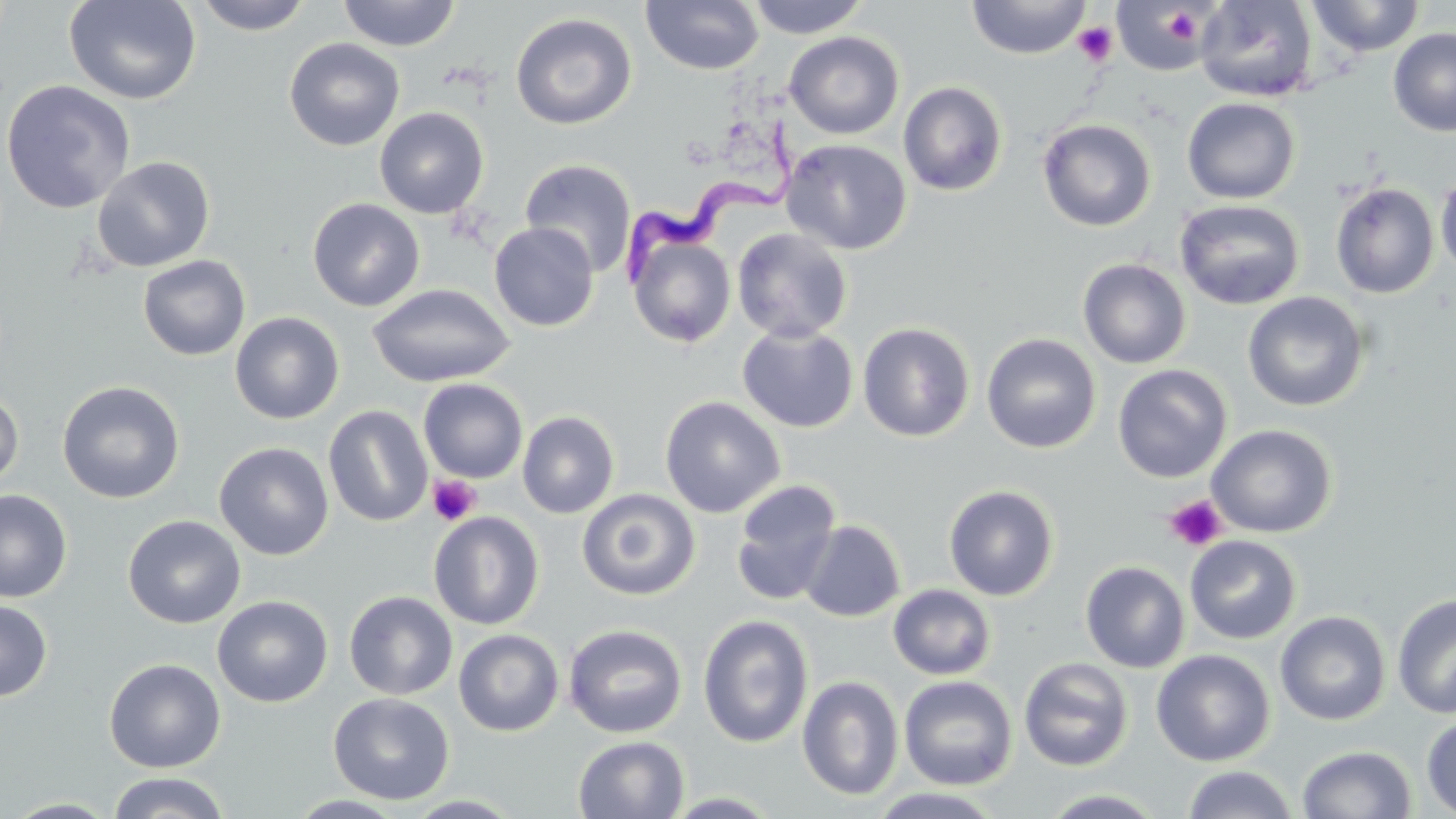

slide_level_diagnosis: Trypanosoma brucei
modality: light microscopy
magnification: 1000x
trypanosoma_brucei_locations: 'approximate bounding boxes as [x1, y1, x2, y2] in pixels: [622, 115, 807, 292]'
field_of_view: one of a larger specimen
preparation: thin blood smear
platelet_locations: 'approximate bounding boxes as [x1, y1, x2, y2] in pixels: [1162, 7, 1203, 47], [1072, 21, 1118, 66], [427, 475, 481, 526], [1164, 495, 1228, 552]'
stain: May-Grünwald-Giemsa
image_size: 1456×819 pixels
uninfected_red_blood_cell_locations: 'approximate bounding boxes as [x1, y1, x2, y2] in pixels: [63, 0, 202, 105], [192, 0, 314, 35], [337, 0, 460, 51], [641, 0, 764, 76], [745, 0, 871, 39], [966, 0, 1091, 60], [1112, 0, 1218, 76], [1194, 0, 1317, 102], [1306, 0, 1425, 57], [510, 12, 637, 130], [1388, 27, 1456, 136], [784, 31, 904, 140], [284, 37, 405, 152], [0, 79, 136, 214], [898, 81, 1008, 196], [1182, 97, 1301, 204], [374, 107, 490, 219], [1037, 118, 1156, 231], [781, 138, 912, 255], [91, 155, 216, 272], [519, 158, 637, 277], [1435, 170, 1456, 278], [1330, 182, 1440, 299], [307, 197, 426, 311], [1174, 198, 1305, 310], [488, 222, 599, 332], [732, 228, 853, 343], [626, 230, 736, 350], [137, 255, 250, 361], [1078, 258, 1192, 369], [367, 282, 515, 388], [1242, 291, 1370, 412], [229, 312, 345, 425], [858, 322, 975, 442], [737, 323, 858, 433], [981, 332, 1101, 453], [1112, 364, 1232, 483], [418, 378, 528, 483], [57, 380, 185, 504], [0, 387, 24, 492], [660, 396, 785, 517], [323, 405, 433, 527], [517, 411, 620, 519], [1207, 423, 1338, 538], [214, 442, 334, 560], [730, 480, 844, 606], [943, 484, 1059, 601], [577, 487, 700, 600], [0, 489, 73, 602], [428, 510, 544, 630], [123, 514, 246, 629], [799, 520, 906, 622], [1184, 535, 1302, 644], [1080, 560, 1190, 673], [888, 584, 997, 680], [344, 590, 458, 700], [1392, 593, 1456, 719], [212, 595, 333, 707], [0, 599, 53, 701], [1275, 610, 1391, 726], [697, 614, 814, 748], [563, 624, 687, 738], [453, 629, 564, 736], [1151, 649, 1275, 766], [103, 657, 226, 773], [1018, 657, 1134, 772], [899, 675, 1018, 790], [798, 676, 904, 800], [328, 692, 454, 805], [1421, 714, 1456, 816], [573, 735, 690, 818], [1297, 745, 1416, 819], [1182, 765, 1298, 819], [106, 772, 232, 819], [866, 787, 1007, 818], [1038, 788, 1170, 818], [661, 791, 784, 818], [286, 794, 409, 818], [4, 798, 122, 818]'